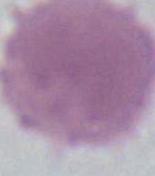
An erythrocyte is seen. Micrograph. 1000x magnification.